Point out each Plasmodium parasite.
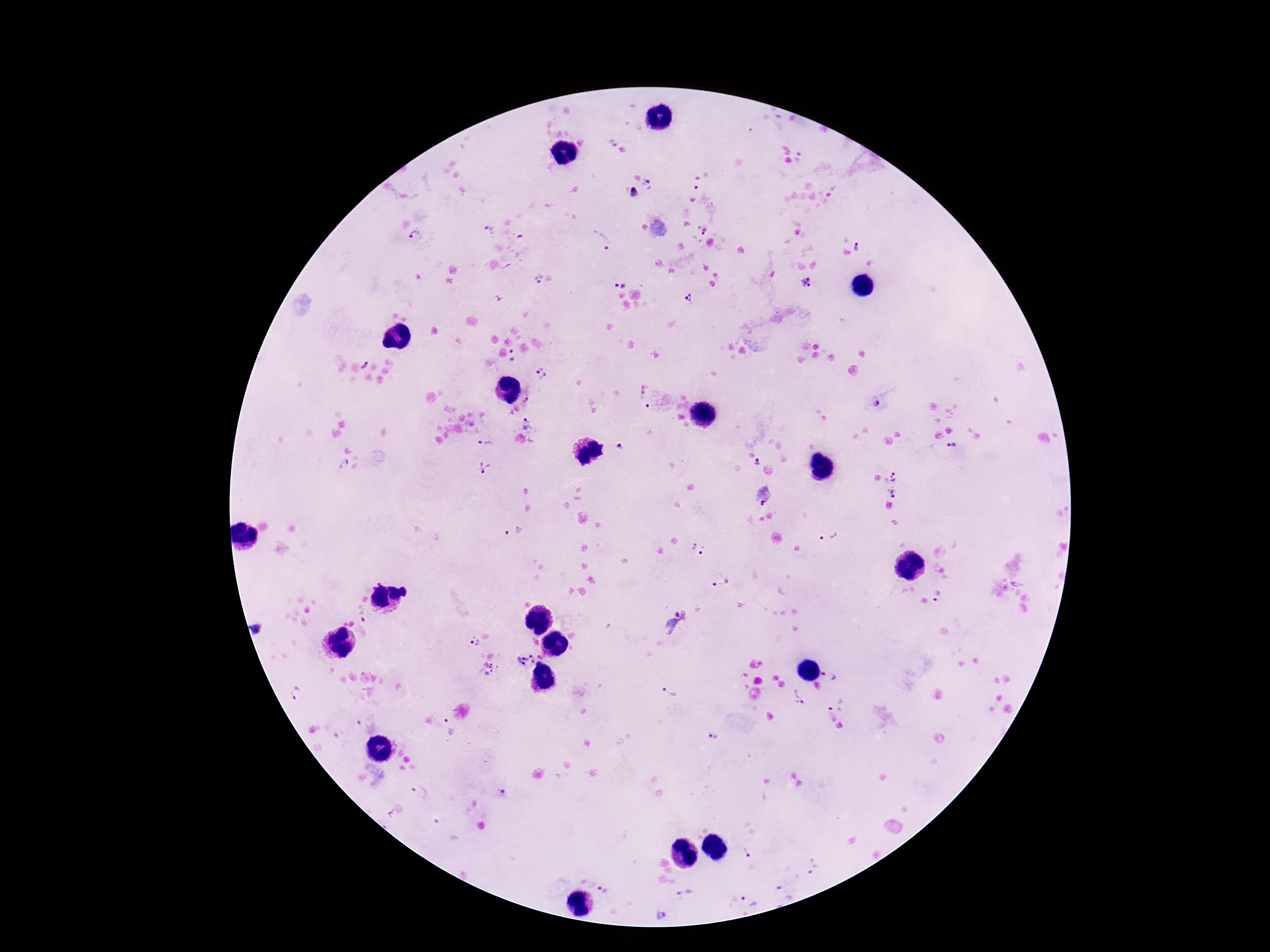

Approximate centers as [x, y] in pixels.
Plasmodium parasites: [614, 145], [701, 174], [691, 192], [633, 193], [703, 228], [488, 232], [418, 235], [602, 242], [858, 246], [537, 277], [805, 280], [619, 284], [689, 298], [513, 355], [363, 365], [541, 373], [644, 400], [877, 404], [528, 423], [484, 441], [621, 446], [952, 446], [758, 463], [344, 464], [484, 468], [895, 474], [894, 492], [763, 494], [514, 532], [829, 536], [698, 551], [721, 583], [938, 598], [360, 613], [475, 643], [524, 659], [489, 666], [829, 677], [669, 694], [296, 695], [798, 696], [835, 702], [447, 727], [713, 734], [419, 791], [747, 855], [813, 869], [604, 889], [684, 893], [784, 893], [750, 900], [660, 914].

Photographed through the microscope eyepiece with a smartphone camera. Thick blood smear. One field from this slide. 100x magnification. Image is 1270×952 pixels. Patient malaria status: positive. Giemsa stain.